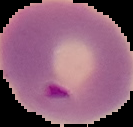

image type = segmented cell region on a black background
result = malaria parasites identified
preparation = thin blood film
image size = 133×127 pixels